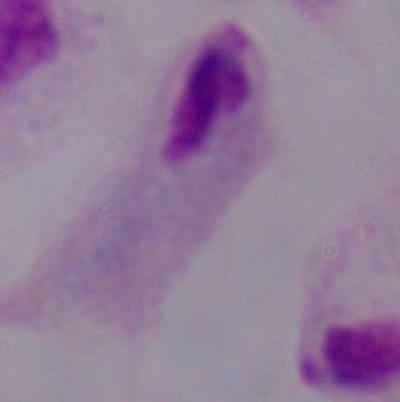
Summary:
  - Identification: trichomonad
  - Magnification: 1000x
  - Modality: photomicrograph